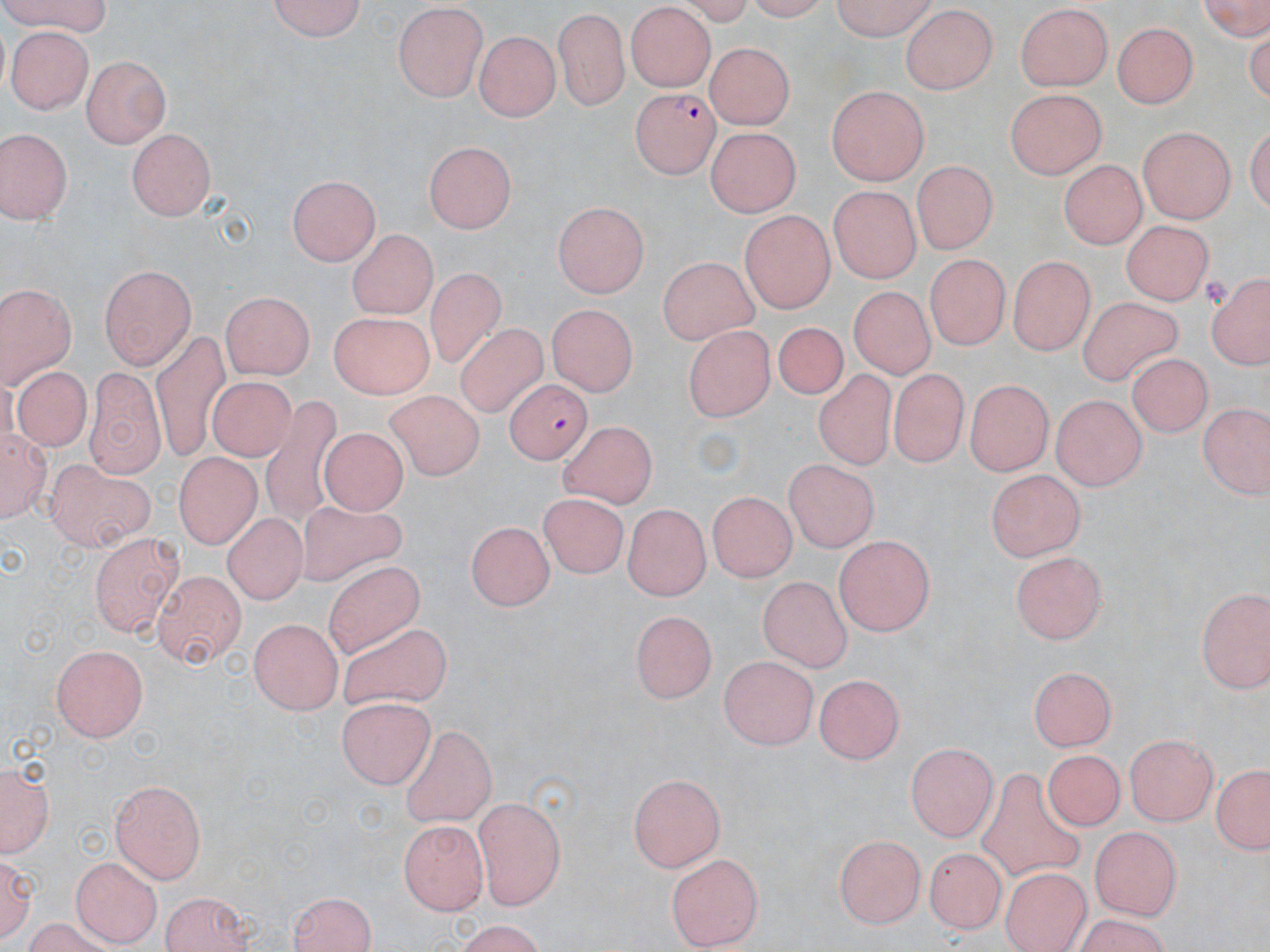 Approximate bounding boxes as (x1,y1)-(x2,y2) corner pairs in pixels. Uninfected red blood cell locations: (0,0)-(114,31), (268,0)-(371,42), (825,0)-(934,38), (1193,0)-(1269,40), (391,4)-(489,99), (1016,4)-(1115,94), (901,6)-(1000,96), (554,7)-(629,111), (625,7)-(718,88), (1115,20)-(1197,107), (7,28)-(93,112), (476,30)-(559,122), (706,41)-(796,127), (81,56)-(170,148), (827,85)-(928,185), (1006,89)-(1102,179), (0,127)-(72,228), (1137,127)-(1234,223), (704,128)-(802,215), (126,130)-(219,224), (420,135)-(516,230), (915,157)-(1000,252), (1060,162)-(1145,246), (288,173)-(381,262), (829,189)-(920,283), (551,195)-(647,295), (739,208)-(834,312), (1119,217)-(1213,303), (347,230)-(437,319), (656,256)-(758,342), (923,257)-(1009,350), (1007,257)-(1093,354), (99,262)-(197,367), (426,268)-(504,373), (1205,272)-(1270,373), (0,283)-(78,386), (848,284)-(962,382), (218,292)-(316,381), (1080,297)-(1184,390), (546,305)-(638,396), (329,314)-(435,403), (776,318)-(851,411), (684,324)-(778,425), (455,325)-(549,416), (149,330)-(231,461), (1125,356)-(1219,436), (85,365)-(172,481), (13,369)-(98,456), (814,369)-(891,471), (892,369)-(967,468), (206,377)-(299,465), (966,377)-(1050,478), (386,390)-(485,480), (263,395)-(342,526), (1049,395)-(1147,491), (1199,405)-(1266,501), (572,422)-(651,514), (0,426)-(54,529), (322,429)-(405,514), (170,446)-(258,548), (43,456)-(161,557), (779,458)-(881,552), (982,469)-(1085,563), (543,487)-(624,575), (708,492)-(796,582), (622,500)-(710,598), (299,503)-(408,588), (220,511)-(312,607), (470,516)-(558,610), (834,531)-(933,636), (90,533)-(184,640), (1008,547)-(1105,643), (323,557)-(426,655), (150,568)-(250,666), (756,574)-(856,672), (1193,581)-(1269,693), (629,608)-(713,704), (249,616)-(344,716), (338,627)-(452,704), (49,642)-(151,743), (718,653)-(815,750), (1027,662)-(1114,750), (819,671)-(908,762), (340,696)-(434,790), (398,724)-(497,827), (1126,733)-(1220,823), (909,740)-(1000,840), (1043,749)-(1128,831), (0,759)-(55,857), (1207,765)-(1270,857), (972,768)-(1089,883), (628,773)-(727,871), (112,779)-(208,883), (472,795)-(567,908), (398,820)-(490,914), (1088,825)-(1181,919), (832,831)-(929,928), (925,847)-(1009,936), (2,852)-(38,938), (665,852)-(765,947), (72,856)-(160,943), (1000,868)-(1094,951), (290,890)-(380,952), (157,891)-(258,951), (443,924)-(556,951). Plasmodium falciparum-infected red blood cell locations: (631,87)-(717,179), (503,379)-(590,464). Slide-level diagnosis: Plasmodium falciparum. Light microscopy. Single field of view. Captured at 1000x magnification. Thin blood film. Image is 1270×952 pixels. May-Grünwald-Giemsa stain.